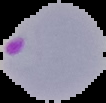

Image is 106×103 pixels. Malaria status: parasitized. Cell region segmented out of the field of view; the surrounding area is masked to black. From a thin blood smear.